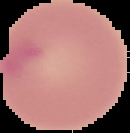

image size = 130×133 pixels
result = no malaria parasites detected
image type = segmented cell region on a black background
preparation = thin blood smear